Report the malaria status of this cell.
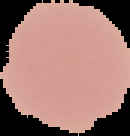
Uninfected.

{
  "preparation": "thin blood smear",
  "image_size": "130×136 pixels",
  "image_type": "segmented cell region with the area outside set to black"
}